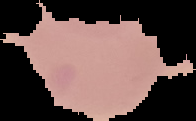
Image is 196×121 pixels. From a thin blood film. Malaria status: uninfected. Segmented cell region on a black background.